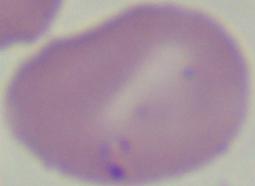
Summary:
  - Magnification: 1000x
  - Identification: Babesia
  - Modality: micrograph